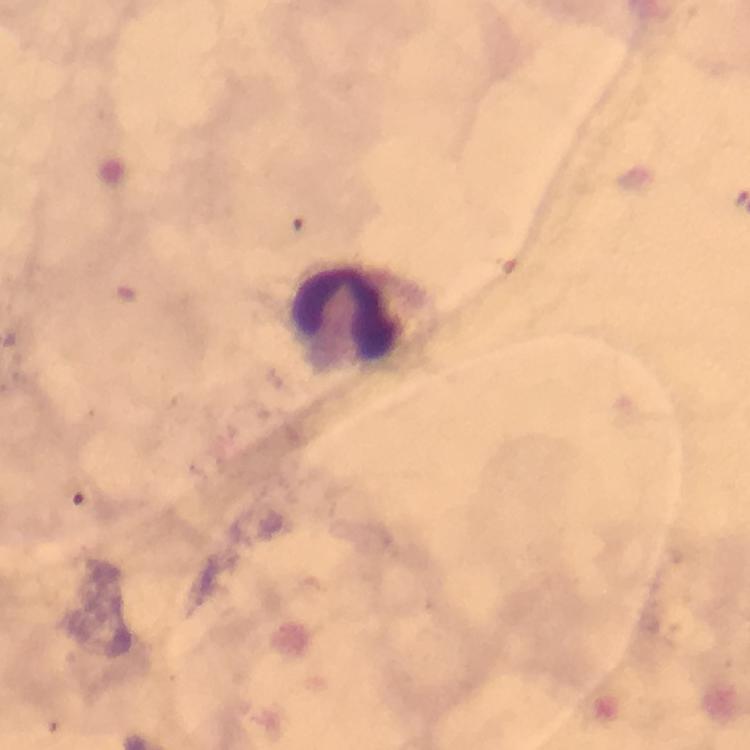
{
  "capture": "smartphone mounted on the microscope",
  "context": "from a diagnostic examination for malaria",
  "immersion_oil": "applied",
  "image_size": "750×750 pixels",
  "leukocyte_locations": "approximate centers as {x, y} in pixels: {351, 317}",
  "malaria_parasites": "none seen",
  "stain": "Giemsa",
  "magnification": "100x",
  "cropped_from": "a single field of view",
  "preparation": "thick blood smear"
}